Report the malaria status of this cell.
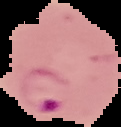

Parasitized.

image type = segmented cell region with the area outside set to black
image size = 121×127 pixels
preparation = thin blood film